Assess this cell for malaria.
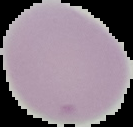
It is uninfected.

Summary:
  - Preparation: thin blood smear
  - Image type: segmented cell region with the area outside set to black
  - Image size: 133×127 pixels